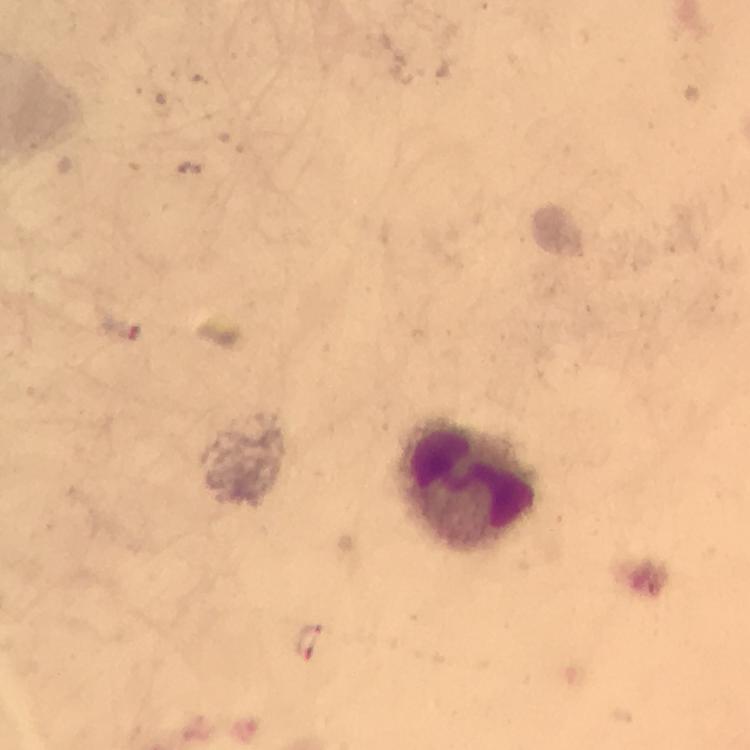
cropped_from: a single field of view
magnification: 100x
stain: Giemsa
immersion_oil: applied
malaria_parasites: none seen
image_size: 750×750 pixels
capture: smartphone camera through the microscope
leukocyte_locations: 'approximate centers as {x, y} in pixels: {466, 482}'
preparation: thick blood film
context: from a diagnostic examination for malaria